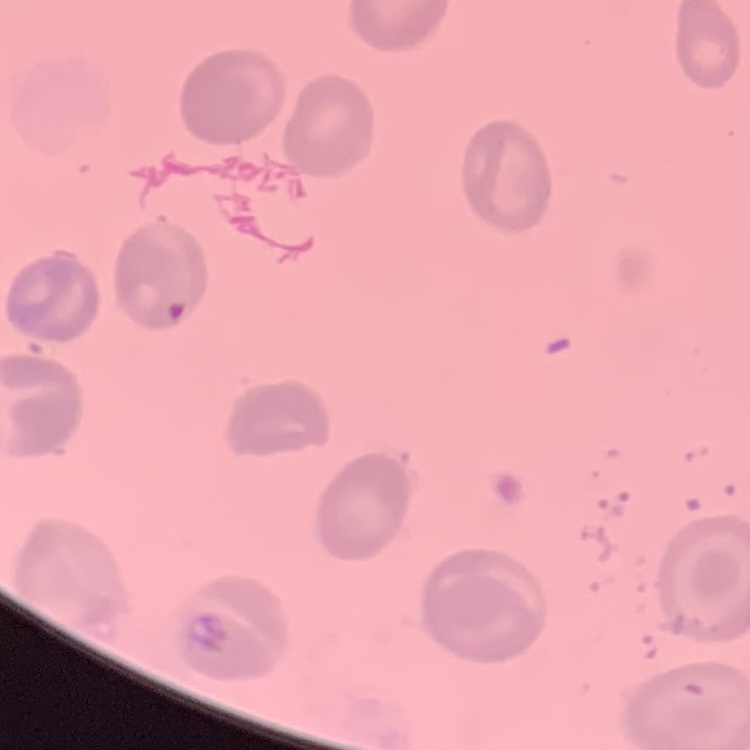

The red blood cells show no rouleaux formation. Thin blood film. Stained with either Field's or Giemsa. One tile cut from a larger photomicrograph.